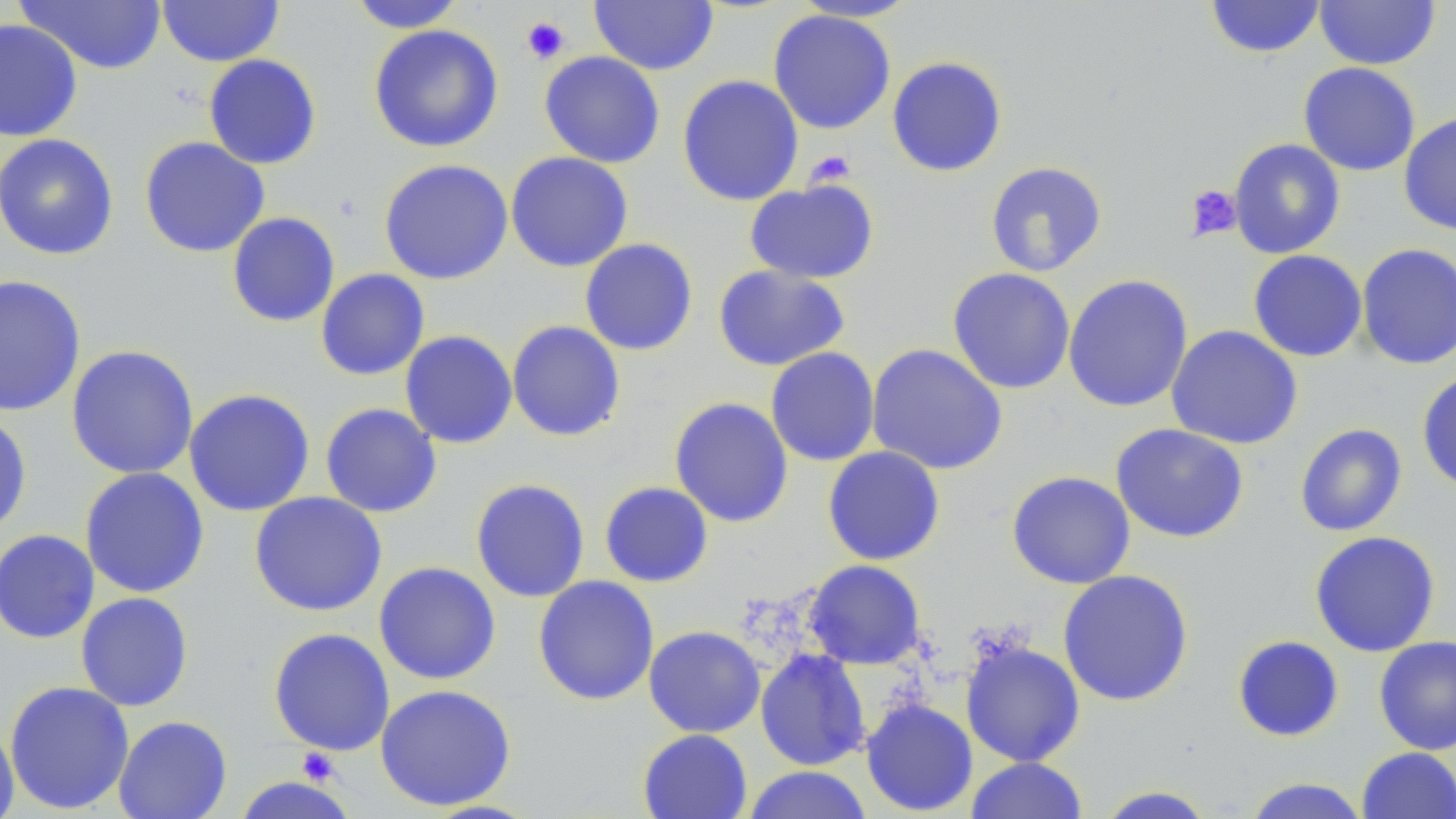

Approximate bounding boxes as (x1, y1, x2, y2) in pixels. Platelet locations: (520, 16, 571, 65), (806, 150, 856, 187), (1185, 184, 1242, 240), (296, 747, 342, 785). Uninfected red blood cell locations: (156, 0, 285, 67), (788, 0, 922, 22), (1205, 0, 1325, 59), (1313, 0, 1441, 70), (14, 1, 167, 75), (347, 1, 467, 33), (588, 1, 719, 75), (768, 9, 896, 135), (0, 18, 83, 142), (368, 24, 504, 153), (539, 51, 666, 169), (203, 54, 322, 170), (886, 56, 1008, 177), (1298, 62, 1421, 176), (677, 74, 804, 206), (1398, 110, 1456, 236), (0, 133, 119, 260), (139, 136, 270, 258), (1228, 138, 1346, 259), (505, 151, 634, 272), (378, 158, 514, 285), (985, 161, 1108, 277), (744, 178, 880, 284), (227, 212, 340, 327), (579, 238, 698, 356), (1357, 243, 1456, 370), (1248, 250, 1367, 362), (712, 265, 850, 371), (947, 267, 1076, 394), (315, 268, 430, 381), (0, 273, 86, 418), (1062, 274, 1193, 413), (507, 320, 626, 442), (1166, 325, 1303, 450), (399, 330, 518, 449), (866, 343, 1008, 475), (66, 344, 199, 480), (765, 346, 880, 466), (1416, 370, 1456, 492), (183, 388, 315, 517), (669, 396, 794, 528), (320, 402, 443, 518), (0, 412, 32, 536), (1110, 423, 1249, 543), (1294, 423, 1408, 537), (822, 446, 946, 566), (79, 467, 210, 599), (1006, 470, 1136, 589), (470, 478, 591, 603), (599, 481, 714, 587), (249, 491, 387, 617), (1, 529, 100, 645), (1309, 530, 1441, 657), (803, 560, 926, 670), (373, 561, 501, 685), (1057, 569, 1194, 707), (532, 575, 660, 706), (76, 592, 194, 711), (643, 625, 766, 738), (268, 627, 395, 755), (1232, 635, 1345, 742), (1373, 635, 1456, 756), (960, 638, 1086, 767), (755, 648, 871, 771), (4, 680, 135, 814), (375, 684, 516, 811), (861, 698, 978, 816), (113, 715, 232, 819), (0, 721, 19, 819), (637, 728, 753, 819), (1357, 746, 1456, 819), (964, 757, 1089, 818), (741, 765, 874, 819), (231, 775, 358, 819), (1241, 778, 1371, 819), (1092, 786, 1220, 818). Slide-level diagnosis: no evidence of blood parasites. One field of a larger specimen. Thin blood smear. Optical microscopy. Image is 1456×819 pixels. 1000x magnification. May-Grünwald-Giemsa stain.